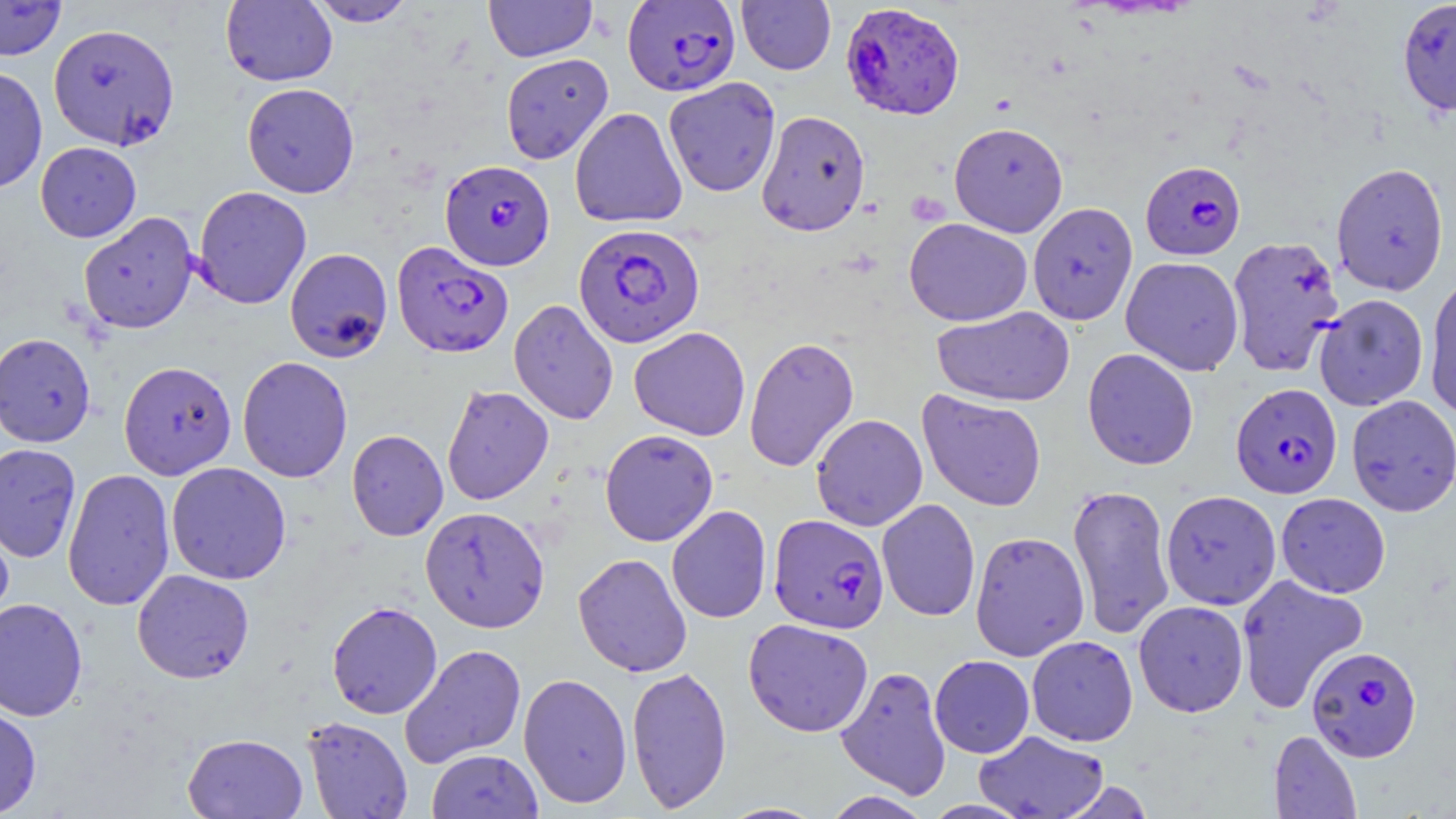

Summary:
  - Coordinate format: approximate bounding boxes as [x1, y1, x2, y2] in pixels
  - Plasmodium falciparum-infected red blood cell locations: [622, 0, 741, 96], [840, 3, 965, 120], [440, 160, 555, 271], [1141, 160, 1246, 260], [573, 223, 704, 348], [1226, 234, 1345, 377], [392, 241, 514, 358], [1230, 383, 1342, 499], [769, 514, 889, 634], [1306, 645, 1422, 762]
  - Uninfected red blood cell locations: [0, 0, 67, 61], [305, 0, 419, 27], [483, 0, 598, 62], [1396, 0, 1456, 117], [221, 1, 337, 87], [736, 1, 836, 75], [48, 23, 180, 150], [501, 53, 613, 165], [0, 66, 48, 194], [663, 77, 781, 197], [242, 82, 360, 197], [570, 106, 687, 228], [756, 110, 871, 236], [949, 121, 1068, 237], [35, 142, 142, 242], [1331, 161, 1450, 296], [193, 186, 312, 309], [1027, 202, 1138, 325], [78, 211, 199, 334], [904, 217, 1032, 326], [284, 247, 393, 363], [1120, 256, 1244, 375], [1424, 272, 1456, 417], [1313, 293, 1429, 411], [508, 299, 619, 425], [931, 306, 1074, 407], [610, 325, 733, 546], [629, 326, 751, 441], [0, 332, 95, 447], [743, 335, 859, 472], [1082, 348, 1199, 470], [237, 356, 353, 483], [118, 360, 237, 479], [441, 384, 554, 505], [917, 389, 1047, 511], [1346, 395, 1456, 516], [810, 413, 928, 531], [347, 429, 448, 541], [600, 429, 718, 546], [0, 443, 82, 563], [166, 462, 292, 585], [62, 468, 175, 611], [1067, 483, 1175, 640], [1160, 489, 1281, 610], [1276, 492, 1391, 597], [877, 498, 980, 621], [666, 505, 772, 624], [420, 506, 550, 633], [0, 513, 15, 628], [970, 530, 1090, 661], [572, 553, 692, 677], [131, 569, 255, 683], [1235, 573, 1369, 714], [0, 597, 88, 722], [1133, 600, 1249, 717], [326, 601, 443, 719], [743, 618, 873, 737], [1027, 636, 1138, 746], [399, 643, 527, 768], [930, 655, 1034, 758], [836, 664, 952, 800], [626, 665, 732, 812], [518, 673, 633, 809], [0, 704, 41, 818], [302, 716, 413, 819], [1268, 730, 1361, 819], [973, 731, 1110, 819], [182, 733, 308, 818], [427, 748, 543, 819], [1058, 780, 1155, 819], [821, 791, 933, 818], [718, 802, 827, 819]
  - Slide-level diagnosis: Plasmodium falciparum
  - Magnification: 1000x
  - Preparation: thin blood film
  - Modality: light microscopy
  - Stain: May-Grünwald-Giemsa
  - Image size: 1456×819 pixels
  - Field of view: one of a larger specimen